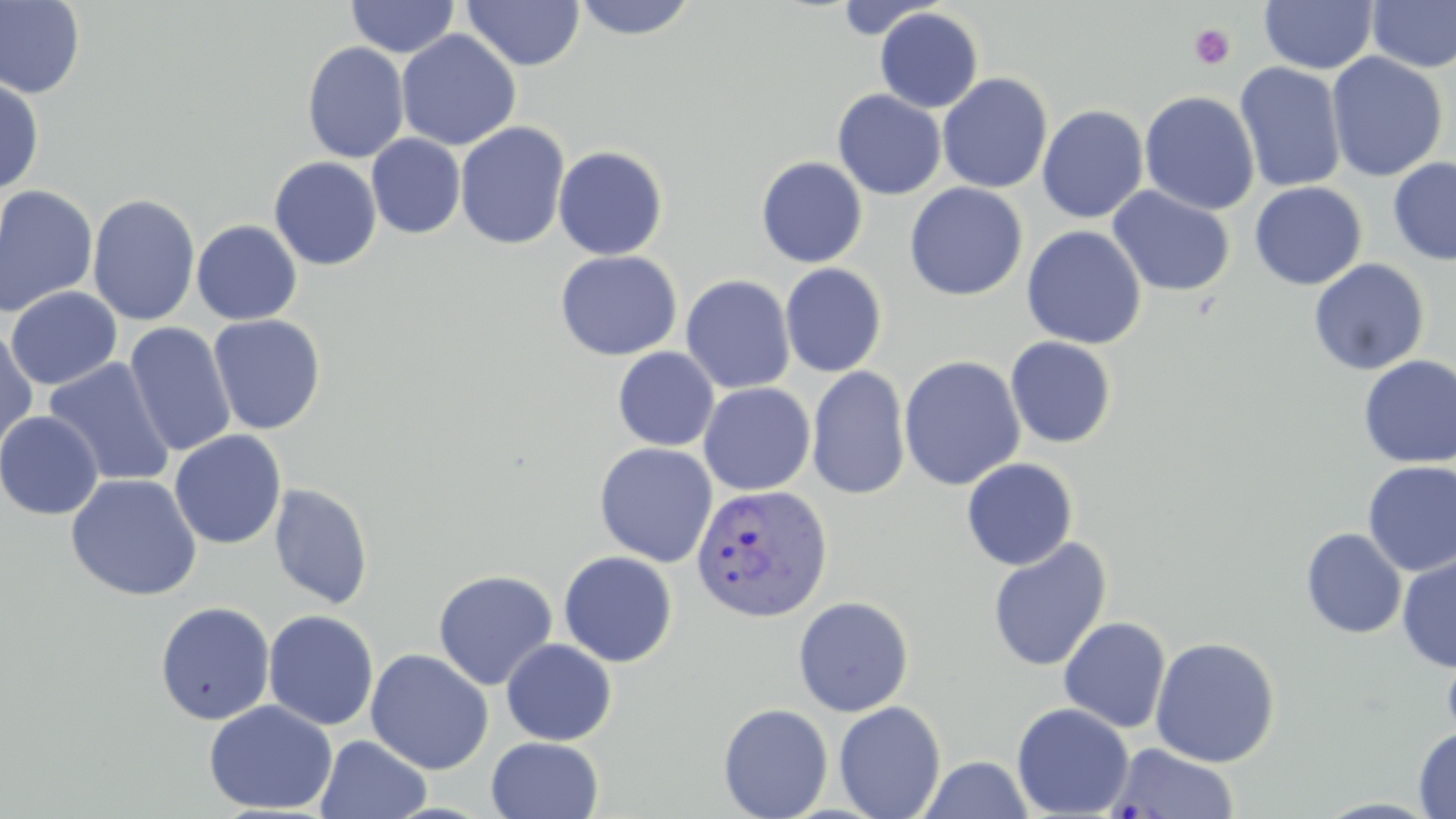
{
  "slide_level_diagnosis": "Plasmodium vivax",
  "magnification": "1000x",
  "field_of_view": "single",
  "platelet_locations": "approximate bounding boxes as [x1, y1, x2, y2] in pixels: [1189, 24, 1236, 70]",
  "preparation": "thin blood smear",
  "uninfected_red_blood_cell_locations": "approximate bounding boxes as [x1, y1, x2, y2] in pixels: [346, 0, 460, 58], [571, 0, 699, 40], [1259, 0, 1378, 75], [0, 1, 86, 98], [462, 1, 585, 71], [1367, 1, 1456, 73], [874, 7, 984, 113], [395, 29, 521, 151], [302, 41, 409, 163], [1326, 52, 1447, 182], [1234, 62, 1347, 193], [936, 72, 1053, 194], [0, 75, 44, 196], [832, 89, 946, 200], [1140, 91, 1260, 216], [1037, 104, 1149, 223], [454, 121, 571, 250], [366, 133, 466, 239], [553, 145, 669, 261], [268, 157, 382, 270], [756, 157, 868, 267], [1388, 157, 1456, 265], [1249, 181, 1367, 290], [904, 182, 1028, 301], [0, 185, 99, 317], [1107, 186, 1236, 297], [87, 193, 201, 326], [191, 220, 303, 325], [1022, 225, 1146, 349], [555, 250, 682, 361], [1308, 258, 1430, 376], [780, 263, 888, 377], [680, 274, 796, 394], [5, 286, 122, 390], [207, 314, 327, 435], [124, 322, 236, 457], [0, 327, 39, 451], [1005, 336, 1117, 449], [612, 347, 719, 451], [898, 355, 1026, 491], [1358, 355, 1456, 468], [42, 358, 176, 487], [806, 365, 911, 501], [698, 382, 816, 496], [0, 411, 104, 520], [169, 430, 287, 550], [594, 442, 718, 567], [961, 457, 1079, 570], [1362, 461, 1456, 577], [65, 473, 202, 602], [269, 483, 373, 610], [1301, 528, 1407, 639], [987, 537, 1112, 673], [558, 550, 678, 667], [1397, 553, 1456, 672], [432, 569, 558, 691], [793, 595, 914, 717], [155, 601, 275, 725], [263, 609, 380, 731], [1058, 616, 1171, 734], [1149, 636, 1281, 767], [500, 639, 617, 746], [1441, 640, 1456, 748], [365, 648, 494, 774], [203, 700, 338, 815], [834, 701, 946, 819], [1011, 702, 1134, 818], [718, 703, 833, 819], [1414, 727, 1456, 818], [315, 734, 431, 819], [486, 736, 604, 819], [1106, 742, 1239, 819], [919, 756, 1033, 818]",
  "stain": "May-Grünwald-Giemsa",
  "image_size": "1456×819 pixels",
  "modality": "light microscopy",
  "plasmodium_vivax_infected_red_blood_cell_locations": "approximate bounding boxes as [x1, y1, x2, y2] in pixels: [691, 482, 834, 623]"
}